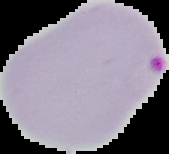
image size = 169×154 pixels
malaria status = parasitized
preparation = thin blood film
image type = cell region segmented out of the field of view; surrounding area masked to black